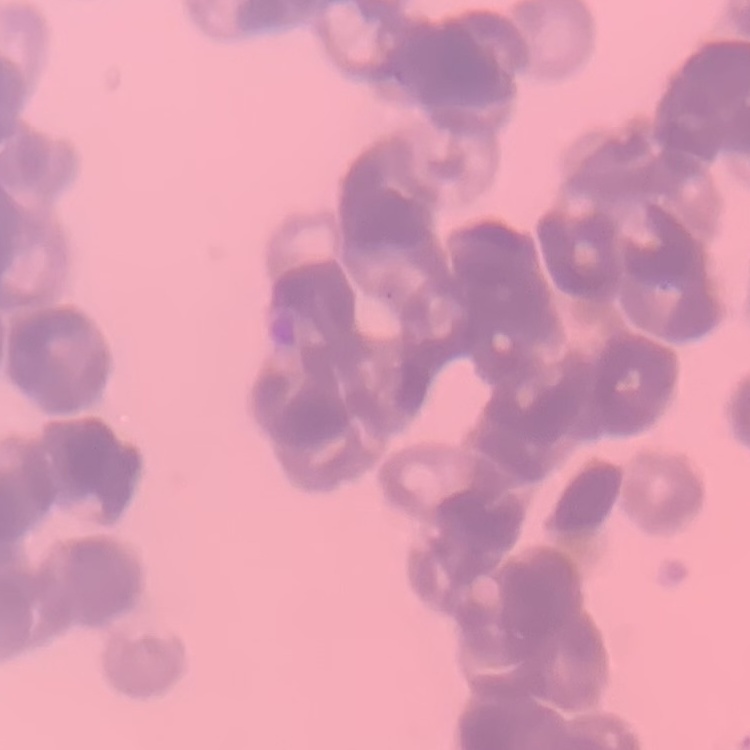

{
  "erythrocyte_morphology": "rouleaux formation",
  "image_type": "square crop of a larger photomicrograph",
  "preparation": "thin peripheral smear",
  "stain": "Field's or Giemsa"
}